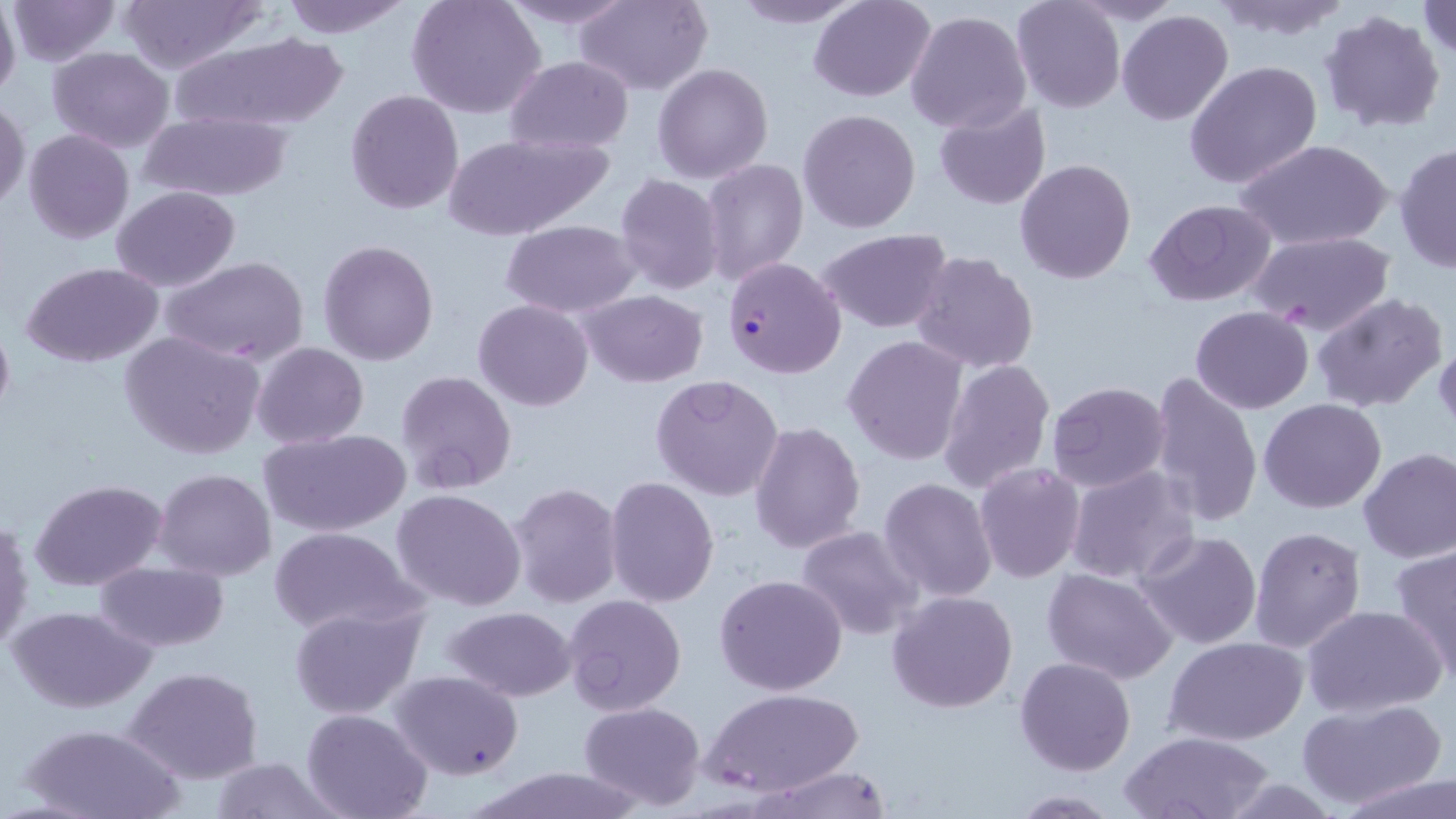

Approximate bounding boxes as [x1, y1, x2, y2] in pixels. Plasmodium falciparum-infected red blood cell locations: [723, 256, 847, 378]. Uninfected red blood cell locations: [6, 0, 121, 66], [114, 0, 267, 71], [279, 0, 416, 39], [405, 0, 545, 119], [497, 0, 638, 29], [576, 0, 712, 95], [729, 0, 865, 28], [808, 0, 934, 101], [1011, 0, 1126, 112], [1417, 0, 1456, 62], [1210, 1, 1356, 43], [0, 2, 21, 101], [905, 8, 1032, 135], [1319, 10, 1446, 135], [1117, 11, 1234, 126], [172, 32, 350, 134], [48, 46, 175, 154], [504, 55, 633, 153], [1185, 60, 1322, 191], [653, 63, 774, 183], [346, 91, 464, 213], [0, 98, 29, 214], [934, 102, 1053, 209], [798, 109, 921, 232], [138, 111, 292, 201], [23, 128, 134, 243], [977, 129, 1106, 274], [440, 133, 609, 239], [1236, 137, 1394, 252], [1393, 144, 1455, 273], [1015, 158, 1138, 284], [702, 159, 808, 285], [614, 174, 725, 295], [108, 186, 240, 292], [1145, 199, 1278, 306], [502, 220, 638, 318], [818, 229, 954, 332], [1248, 231, 1396, 336], [317, 239, 440, 366], [910, 251, 1039, 374], [164, 257, 308, 365], [21, 262, 165, 366], [580, 290, 708, 387], [1312, 291, 1448, 412], [473, 298, 593, 411], [1190, 306, 1313, 414], [0, 310, 14, 430], [120, 331, 265, 461], [843, 336, 968, 466], [251, 341, 369, 449], [1433, 342, 1456, 434], [935, 356, 1054, 494], [395, 371, 518, 497], [1147, 371, 1264, 530], [651, 375, 785, 501], [1046, 382, 1171, 494], [1259, 397, 1386, 513], [749, 422, 866, 553], [258, 428, 412, 538], [1358, 448, 1456, 564], [973, 462, 1087, 584], [1065, 466, 1198, 587], [152, 468, 276, 580], [604, 477, 719, 607], [29, 478, 167, 591], [879, 478, 999, 603], [508, 483, 624, 609], [392, 489, 526, 611], [1, 517, 33, 653], [1247, 525, 1365, 653], [797, 526, 922, 640], [269, 528, 420, 637], [1132, 528, 1263, 650], [1390, 545, 1456, 684], [96, 562, 229, 653], [1041, 568, 1178, 683], [715, 573, 848, 697], [888, 590, 1018, 713], [561, 594, 687, 718], [1301, 603, 1447, 717], [289, 604, 424, 718], [9, 605, 154, 713], [441, 606, 578, 702], [1165, 637, 1308, 746], [1015, 656, 1136, 776], [122, 665, 264, 783], [391, 670, 523, 780], [703, 688, 859, 797], [1298, 699, 1446, 809], [578, 700, 705, 809], [302, 709, 433, 819], [19, 721, 183, 819], [1120, 730, 1274, 818], [212, 755, 338, 819], [751, 764, 896, 819], [471, 768, 648, 819], [1341, 773, 1456, 819], [1010, 791, 1120, 817]. Slide-level diagnosis: Plasmodium falciparum. May-Grünwald-Giemsa stain. Optical microscopy. Thin blood film. One field of a larger specimen. Captured at 1000x magnification. Image is 1456×819 pixels.